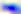
{
  "identification": "Toxoplasma gondii",
  "magnification": "400x",
  "modality": "micrograph"
}